Locate and identify every blood parasite.
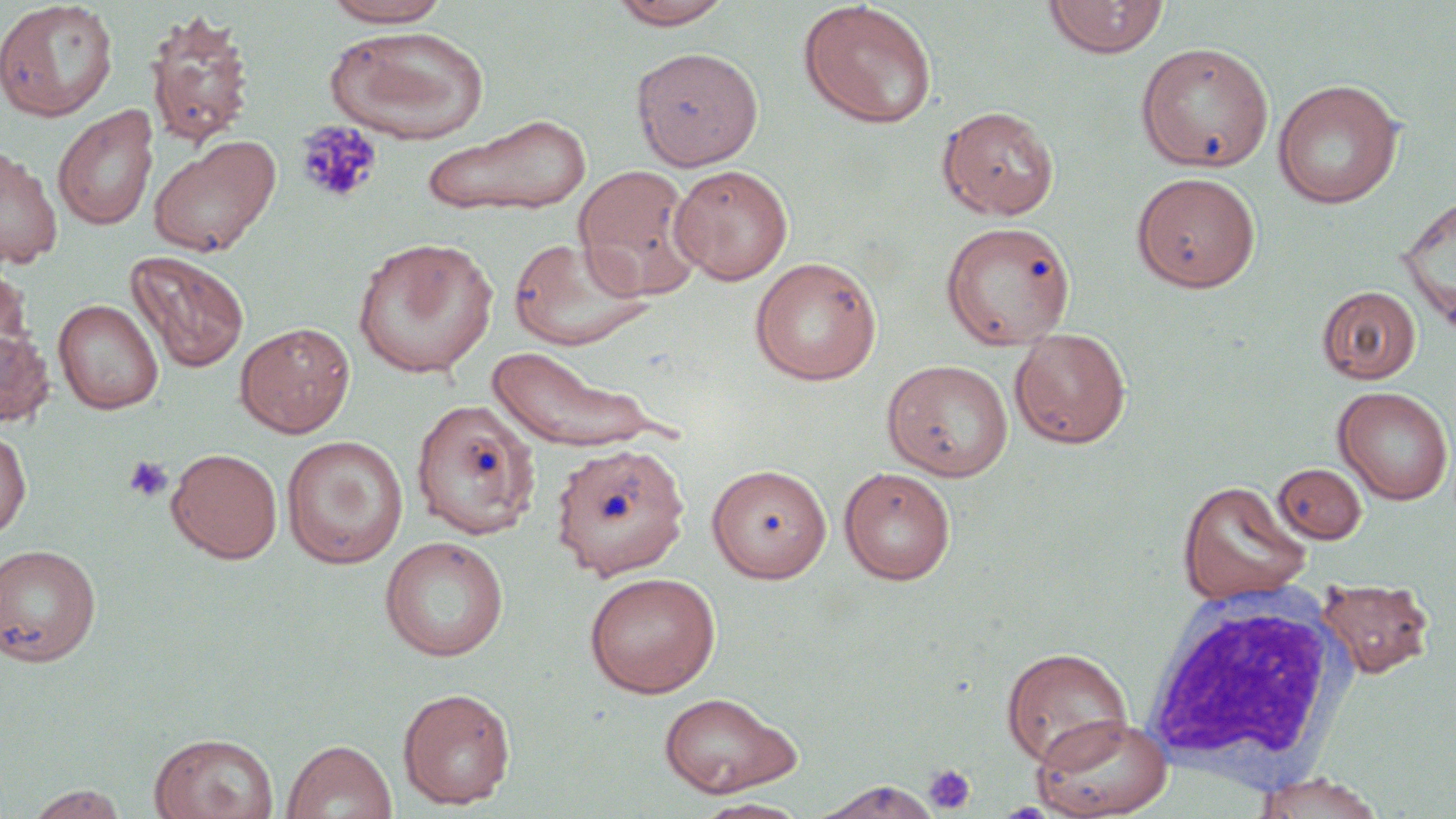

No blood parasites observed.

Approximate bounding boxes as [x1, y1, x2, y2] in pixels. White blood cell locations: [1136, 593, 1355, 793]. Platelet locations: [294, 120, 383, 205], [123, 455, 172, 502], [923, 763, 977, 815]. Uninfected red blood cell locations: [319, 0, 453, 27], [608, 0, 736, 29], [1043, 0, 1169, 59], [0, 1, 118, 121], [798, 1, 938, 128], [143, 9, 256, 149], [325, 25, 490, 144], [1135, 41, 1274, 172], [631, 47, 763, 169], [1272, 79, 1403, 209], [52, 104, 159, 231], [938, 105, 1059, 219], [422, 113, 592, 215], [147, 134, 281, 257], [0, 145, 63, 269], [572, 163, 703, 300], [669, 164, 793, 285], [1131, 171, 1261, 292], [1397, 192, 1456, 332], [940, 221, 1076, 349], [507, 236, 653, 351], [351, 237, 500, 378], [126, 250, 250, 373], [749, 256, 882, 385], [0, 261, 32, 363], [1317, 285, 1421, 384], [53, 299, 163, 414], [235, 321, 356, 438], [0, 325, 55, 427], [1009, 327, 1131, 449], [487, 344, 666, 452], [882, 359, 1014, 481], [1333, 386, 1454, 505], [410, 398, 542, 540], [0, 425, 31, 540], [281, 435, 408, 568], [551, 441, 691, 580], [166, 447, 283, 563], [707, 463, 833, 583], [1273, 463, 1367, 544], [838, 466, 956, 585], [1176, 479, 1311, 605], [378, 535, 510, 661], [0, 543, 101, 666], [583, 571, 721, 697], [1316, 578, 1434, 679], [1001, 646, 1133, 770], [397, 687, 516, 809], [657, 691, 801, 798], [1032, 713, 1174, 819], [149, 732, 279, 819], [282, 739, 397, 819], [1250, 774, 1386, 817], [815, 781, 943, 818], [26, 785, 129, 818], [694, 798, 810, 819]. Slide-level diagnosis: no evidence of blood parasites. Thin blood film. Image is 1456×819 pixels. Captured at 1000x magnification. Light microscopy. One field of a larger specimen. May-Grünwald-Giemsa-stained preparation.